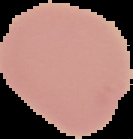

preparation = thin blood smear
image size = 133×139 pixels
malaria status = uninfected
image type = segmented cell region with the area outside set to black